Classify this cell by malaria status.
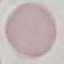
Uninfected.

Automatically extracted cell patch, resized to 64 × 64 pixels. Thin blood film. Acquired by smartphone through the microscope eyepiece. Giemsa stain.